Outline each blood parasite and name the species.
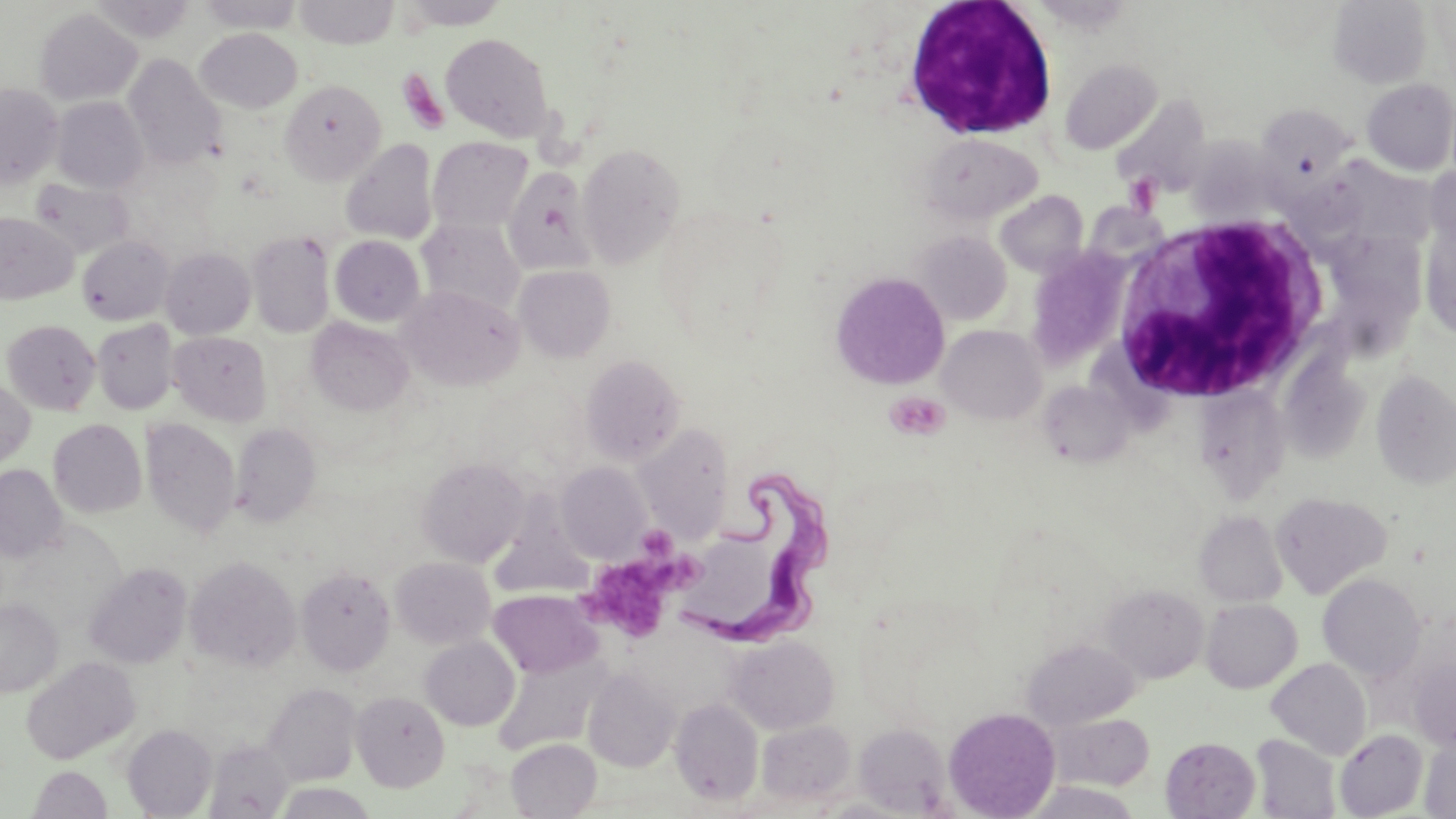
Approximate bounding boxes as named x1/y1/x2/y2 corners in pixels.
Trypanosoma brucei: (x1=678, y1=464, x2=846, y2=651).
No Plasmodium falciparum, Plasmodium ovale, Plasmodium malariae, Plasmodium vivax, or Babesia divergens observed.

slide-level diagnosis = Trypanosoma brucei
white blood cell locations = approximate bounding boxes as named x1/y1/x2/y2 corners in pixels: (x1=901, y1=1, x2=1059, y2=142), (x1=1110, y1=214, x2=1331, y2=403)
uninfected red blood cell locations = approximate bounding boxes as named x1/y1/x2/y2 corners in pixels: (x1=87, y1=0, x2=198, y2=43), (x1=195, y1=0, x2=303, y2=33), (x1=294, y1=0, x2=399, y2=49), (x1=395, y1=0, x2=510, y2=31), (x1=1328, y1=1, x2=1433, y2=88), (x1=34, y1=8, x2=142, y2=106), (x1=195, y1=28, x2=303, y2=113), (x1=440, y1=32, x2=553, y2=142), (x1=123, y1=53, x2=226, y2=170), (x1=1059, y1=59, x2=1161, y2=154), (x1=1361, y1=78, x2=1456, y2=175), (x1=280, y1=79, x2=385, y2=184), (x1=0, y1=83, x2=64, y2=187), (x1=1112, y1=95, x2=1213, y2=198), (x1=50, y1=96, x2=148, y2=193), (x1=1256, y1=103, x2=1356, y2=189), (x1=920, y1=134, x2=1042, y2=225), (x1=1184, y1=135, x2=1285, y2=225), (x1=428, y1=137, x2=532, y2=233), (x1=340, y1=139, x2=439, y2=245), (x1=578, y1=143, x2=685, y2=267), (x1=1426, y1=164, x2=1456, y2=252), (x1=503, y1=166, x2=599, y2=276), (x1=29, y1=177, x2=134, y2=258), (x1=995, y1=191, x2=1089, y2=277), (x1=0, y1=212, x2=78, y2=304), (x1=1419, y1=218, x2=1456, y2=341), (x1=417, y1=219, x2=524, y2=317), (x1=1335, y1=222, x2=1429, y2=325), (x1=247, y1=230, x2=335, y2=338), (x1=911, y1=231, x2=1012, y2=326), (x1=330, y1=235, x2=425, y2=326), (x1=77, y1=236, x2=174, y2=325), (x1=161, y1=247, x2=256, y2=339), (x1=513, y1=265, x2=616, y2=362), (x1=830, y1=271, x2=950, y2=389), (x1=400, y1=285, x2=524, y2=391), (x1=307, y1=317, x2=415, y2=414), (x1=2, y1=319, x2=101, y2=415), (x1=92, y1=319, x2=179, y2=415), (x1=937, y1=324, x2=1046, y2=425), (x1=168, y1=331, x2=271, y2=426), (x1=579, y1=354, x2=686, y2=465), (x1=1278, y1=357, x2=1371, y2=465), (x1=1370, y1=370, x2=1456, y2=488), (x1=0, y1=375, x2=36, y2=472), (x1=1040, y1=382, x2=1134, y2=467), (x1=1194, y1=387, x2=1292, y2=502), (x1=48, y1=418, x2=147, y2=518), (x1=141, y1=418, x2=241, y2=539), (x1=230, y1=421, x2=322, y2=527), (x1=635, y1=425, x2=733, y2=544), (x1=416, y1=456, x2=529, y2=567), (x1=557, y1=462, x2=652, y2=563), (x1=0, y1=464, x2=68, y2=562), (x1=495, y1=482, x2=607, y2=599), (x1=1270, y1=491, x2=1392, y2=599), (x1=1195, y1=510, x2=1288, y2=607), (x1=690, y1=531, x2=780, y2=631), (x1=185, y1=556, x2=301, y2=673), (x1=391, y1=557, x2=495, y2=649), (x1=84, y1=563, x2=192, y2=669), (x1=296, y1=567, x2=395, y2=675), (x1=1318, y1=573, x2=1426, y2=682), (x1=1101, y1=585, x2=1209, y2=684), (x1=489, y1=590, x2=602, y2=678), (x1=0, y1=597, x2=64, y2=697), (x1=1201, y1=599, x2=1302, y2=693), (x1=725, y1=635, x2=839, y2=734), (x1=420, y1=637, x2=519, y2=731), (x1=1022, y1=640, x2=1140, y2=728), (x1=493, y1=647, x2=613, y2=755), (x1=20, y1=656, x2=140, y2=765), (x1=1409, y1=656, x2=1456, y2=751), (x1=1267, y1=658, x2=1371, y2=759), (x1=584, y1=667, x2=680, y2=772), (x1=263, y1=683, x2=363, y2=785), (x1=352, y1=691, x2=449, y2=791), (x1=670, y1=697, x2=764, y2=806), (x1=943, y1=707, x2=1061, y2=819), (x1=1050, y1=712, x2=1155, y2=790), (x1=757, y1=720, x2=855, y2=806), (x1=855, y1=723, x2=951, y2=815), (x1=122, y1=724, x2=217, y2=817), (x1=1335, y1=729, x2=1428, y2=818), (x1=1252, y1=733, x2=1341, y2=818), (x1=1160, y1=737, x2=1260, y2=818), (x1=1421, y1=738, x2=1456, y2=817), (x1=506, y1=739, x2=601, y2=818), (x1=204, y1=740, x2=293, y2=817), (x1=28, y1=765, x2=112, y2=818), (x1=1023, y1=781, x2=1144, y2=819), (x1=273, y1=783, x2=378, y2=819)
preparation = thin blood smear
modality = optical microscopy
magnification = 1000x
platelet locations = approximate bounding boxes as named x1/y1/x2/y2 corners in pixels: (x1=397, y1=68, x2=450, y2=135), (x1=886, y1=392, x2=949, y2=439), (x1=635, y1=524, x2=677, y2=561), (x1=579, y1=535, x2=709, y2=643)
field of view = one of a larger specimen
stain = May-Grünwald-Giemsa
image size = 1456×819 pixels